Assess this cell for malaria.
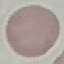
Uninfected.

Summary:
  - Image type: automatically extracted cell patch, resized to 64 × 64 pixels
  - Capture: smartphone through the microscope eyepiece
  - Preparation: thin blood film
  - Stain: Giemsa